Locate and identify every blood parasite.
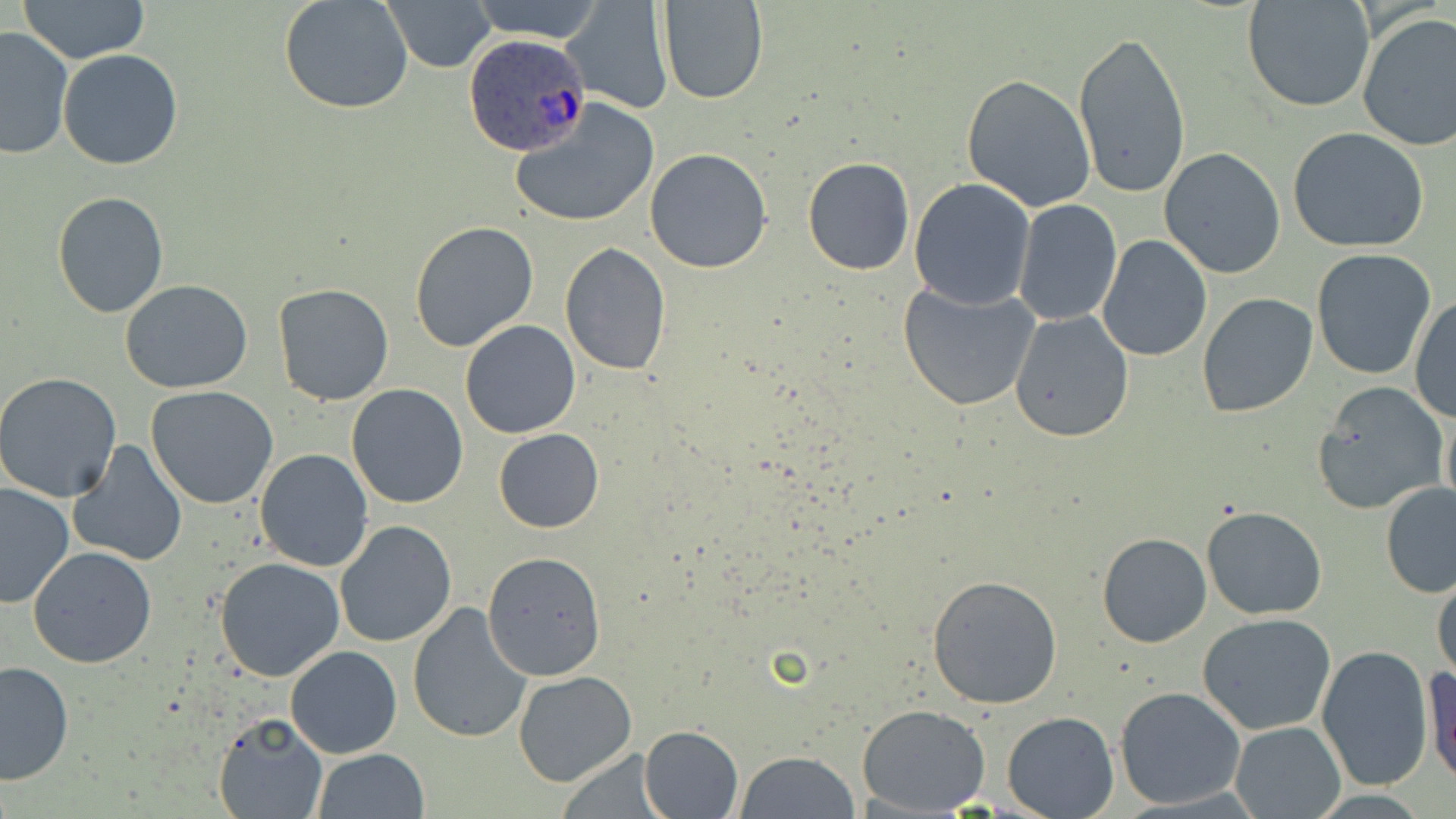

Approximate bounding boxes as [x1, y1, x2, y2] in pixels.
Plasmodium ovale-infected red blood cells: [462, 33, 594, 155].
No Plasmodium falciparum, Plasmodium malariae, Plasmodium vivax, Babesia divergens, or Trypanosoma brucei observed.

slide-level diagnosis = Plasmodium ovale
field of view = one of a larger specimen
stain = May-Grünwald-Giemsa
magnification = 1000x
modality = light microscopy
preparation = thin blood film
uninfected red blood cell locations = approximate bounding boxes as [x1, y1, x2, y2] in pixels: [18, 0, 149, 65], [279, 0, 414, 116], [380, 0, 497, 72], [1242, 0, 1375, 113], [463, 1, 610, 42], [656, 1, 771, 105], [563, 5, 672, 111], [1356, 11, 1456, 156], [0, 26, 76, 160], [1072, 28, 1191, 200], [58, 49, 183, 170], [961, 74, 1096, 211], [512, 97, 661, 228], [1287, 126, 1430, 252], [1159, 147, 1285, 277], [645, 148, 772, 274], [802, 156, 916, 275], [908, 177, 1036, 309], [53, 190, 168, 319], [1013, 199, 1122, 326], [408, 220, 541, 355], [1096, 235, 1212, 361], [559, 243, 672, 377], [1311, 250, 1435, 378], [120, 279, 254, 394], [897, 281, 1040, 411], [272, 283, 395, 408], [1197, 293, 1318, 419], [1410, 297, 1456, 422], [1010, 309, 1135, 442], [460, 319, 580, 438], [0, 371, 123, 502], [1313, 382, 1447, 511], [346, 383, 470, 509], [145, 386, 279, 509], [494, 428, 603, 533], [67, 441, 188, 568], [254, 448, 375, 572], [0, 481, 76, 609], [1380, 483, 1456, 596], [1201, 505, 1328, 620], [333, 520, 456, 649], [1096, 522, 1324, 635], [1096, 532, 1213, 648], [28, 546, 157, 668], [480, 550, 606, 682], [213, 557, 347, 682], [1432, 567, 1456, 682], [927, 573, 1063, 709], [406, 601, 532, 743], [1198, 613, 1335, 736], [286, 645, 402, 758], [1315, 645, 1434, 789], [0, 660, 76, 785], [1422, 663, 1455, 788], [513, 670, 637, 786], [1115, 686, 1246, 810], [859, 704, 991, 815], [1001, 711, 1119, 819], [211, 713, 327, 819], [1229, 720, 1345, 819], [640, 725, 744, 817], [311, 748, 431, 819], [734, 751, 860, 819]
image size = 1456×819 pixels